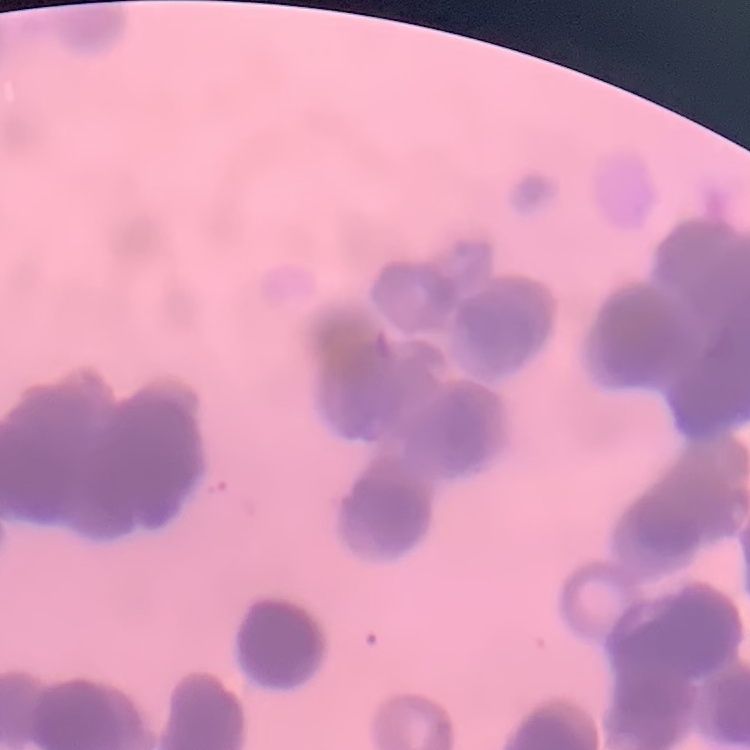
{
  "erythrocyte_morphology": "rouleaux formation",
  "stain": "Field's or Giemsa",
  "image_type": "one tile cut from a larger photomicrograph",
  "preparation": "thin blood film"
}